Outline each uninfected red blood cell.
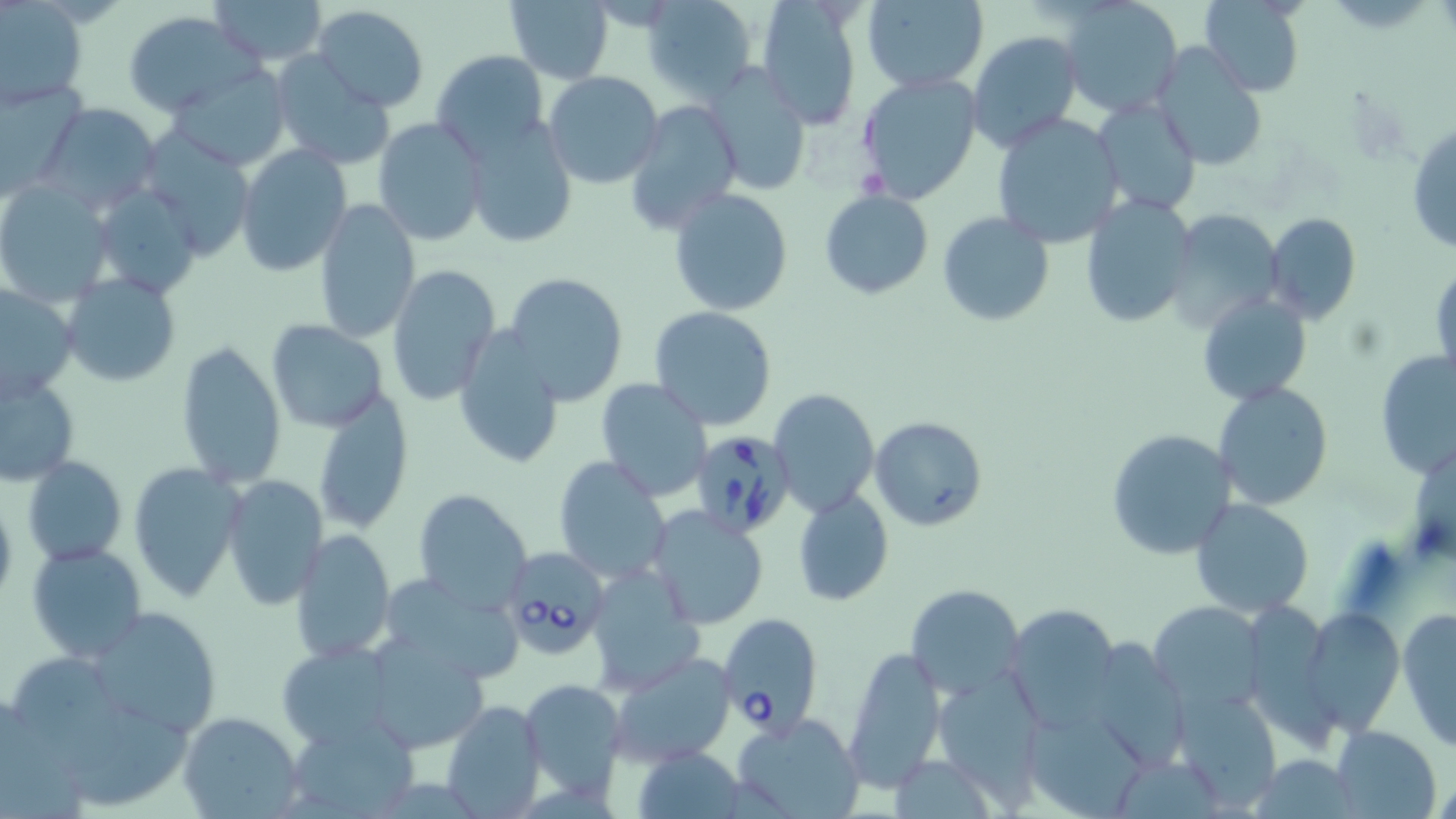
Approximate bounding boxes as (x1,y1)-(x2,y2) corner pairs in pixels.
Uninfected red blood cells: (210,0)-(331,65), (643,0)-(760,101), (860,0)-(989,91), (504,1)-(615,83), (1197,1)-(1306,95), (755,2)-(863,128), (1061,2)-(1181,117), (1,3)-(88,107), (313,6)-(429,113), (123,12)-(257,116), (967,29)-(1082,152), (1152,43)-(1269,171), (431,48)-(551,156), (268,51)-(394,169), (168,62)-(291,170), (701,63)-(811,197), (543,71)-(667,191), (856,72)-(984,206), (0,76)-(86,195), (1093,97)-(1202,217), (623,100)-(742,234), (38,102)-(161,212), (993,113)-(1123,249), (461,116)-(578,247), (372,118)-(487,245), (1407,122)-(1456,257), (234,144)-(352,276), (0,179)-(114,306), (92,182)-(202,300), (668,188)-(794,317), (819,190)-(934,299), (1080,195)-(1197,328), (313,200)-(421,344), (1164,209)-(1284,334), (938,212)-(1054,328), (1264,213)-(1362,324), (1430,260)-(1455,388), (385,264)-(501,405), (504,271)-(629,406), (63,273)-(182,386), (0,284)-(77,404), (1197,292)-(1313,407), (649,305)-(780,430), (267,320)-(388,433), (451,327)-(566,469), (176,339)-(286,488), (1377,350)-(1455,481), (1,370)-(79,487), (594,378)-(714,502), (1213,381)-(1334,510), (309,388)-(415,535), (769,389)-(879,517), (870,417)-(990,532), (1105,428)-(1236,561), (24,455)-(126,566), (553,456)-(671,584), (130,461)-(245,600), (222,474)-(329,608), (413,487)-(535,612), (793,489)-(893,606), (0,493)-(18,608), (1191,497)-(1315,617), (645,505)-(772,629), (289,530)-(396,663), (26,542)-(147,663), (585,568)-(703,692), (389,575)-(523,679), (905,583)-(1023,698), (1149,601)-(1266,711), (1005,603)-(1120,728), (84,606)-(223,740), (1302,606)-(1405,734), (1398,606)-(1456,749), (366,631)-(491,753), (1081,639)-(1190,773), (277,641)-(398,748), (844,647)-(947,791), (608,650)-(736,766), (16,656)-(195,804), (938,668)-(1044,812), (517,677)-(628,803), (1174,688)-(1278,811), (442,699)-(546,816), (1024,707)-(1149,818), (179,711)-(304,819), (730,712)-(867,819), (288,716)-(416,817), (1332,726)-(1441,817), (633,745)-(745,819), (1255,755)-(1357,818).

Babesia divergens-infected red blood cell locations: (690,431)-(795,538), (512,548)-(605,654), (718,612)-(822,736). Slide-level diagnosis: Babesia divergens. 1000x magnification. Image is 1456×819 pixels. One field of a larger specimen. Thin blood smear. Light microscopy. May-Grünwald-Giemsa stain.